Give the position of every Plasmodium parasite visible.
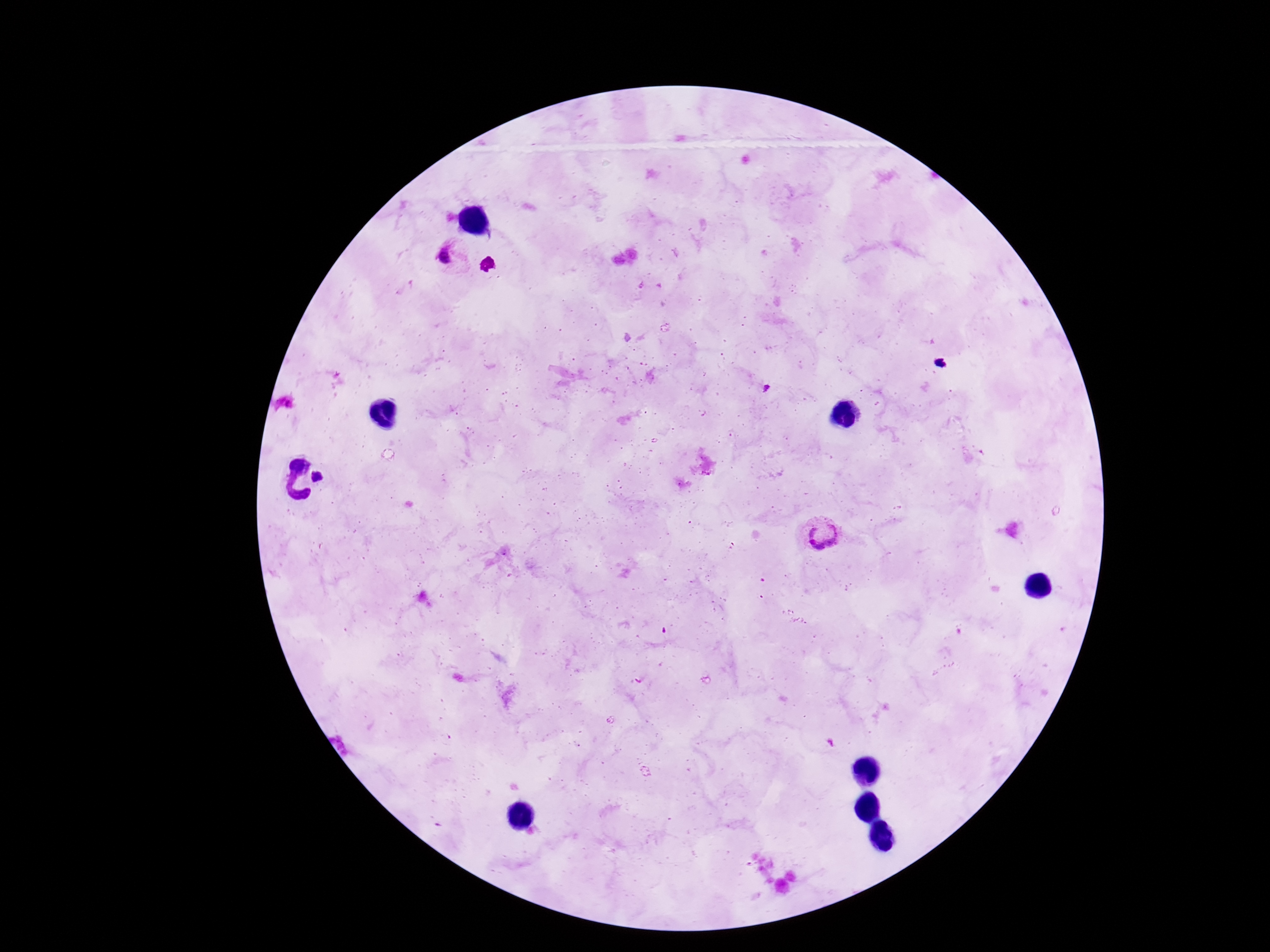
Approximate centers as [x, y] in pixels.
Plasmodium parasites: [449, 258], [940, 363], [321, 478], [822, 535].

Summary:
  - Field of view: one from this slide
  - Patient malaria status: positive
  - Image size: 1270×952 pixels
  - Capture: smartphone camera through the microscope eyepiece
  - Magnification: 100x
  - Preparation: thick blood film
  - Stain: Giemsa